Name the parasite shown.
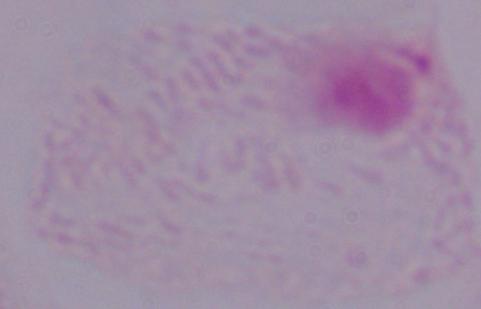

This is a trichomonad.

{
  "modality": "photomicrograph",
  "magnification": "1000x"
}